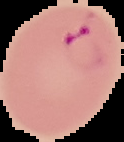
image_size: 124×142 pixels
preparation: thin blood smear
image_type: cell region segmented out of the field of view; surrounding area masked to black
result: Plasmodium parasites detected